Assess for malaria.
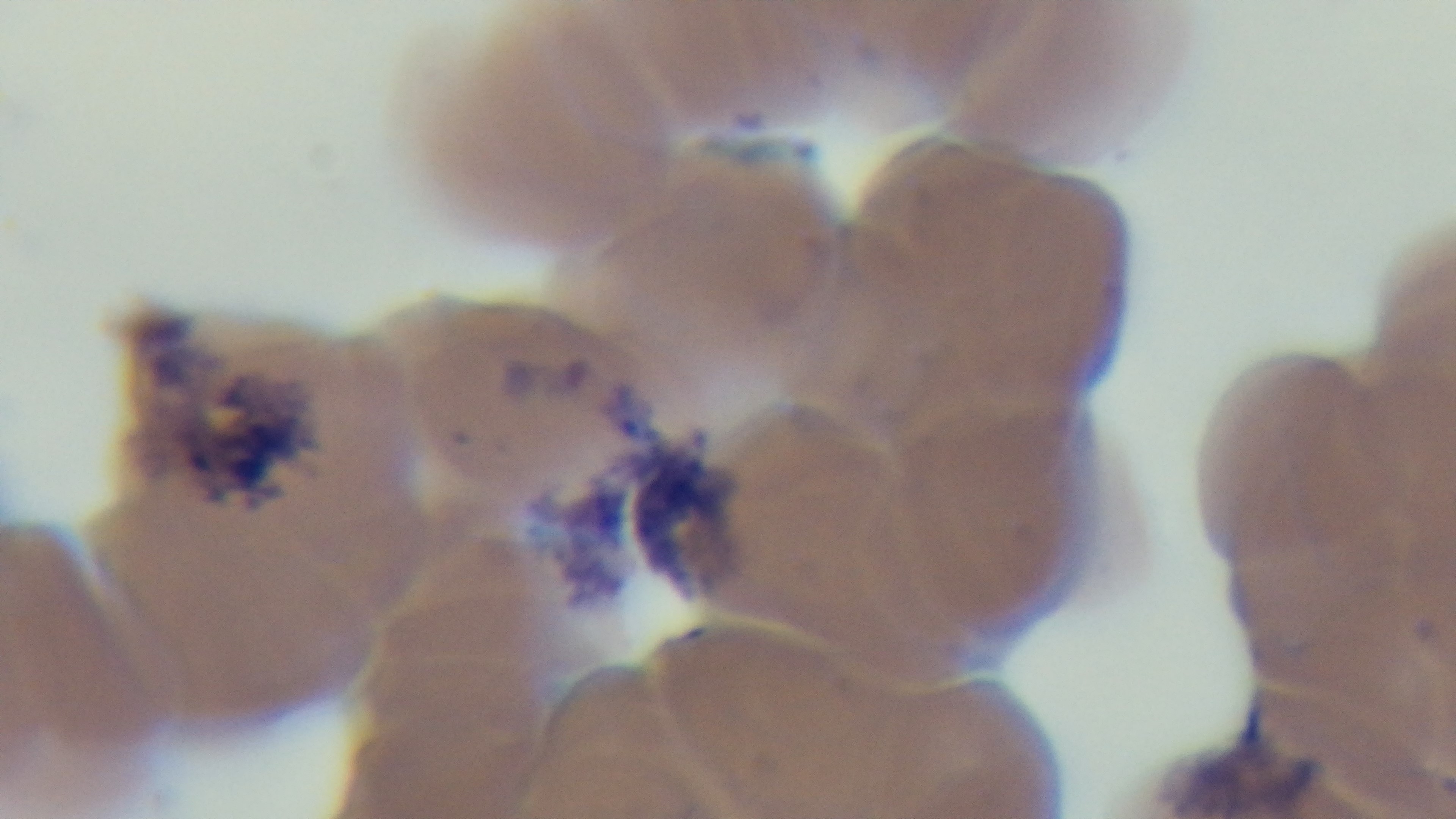

Infected.

modality = light microscopy
capture = mounted 4K digital camera
objective = 100x oil immersion
preparation = thin smear
stain = Giemsa
field of view = single